Give the extent of all Plasmodium ovale-infected red blood cells.
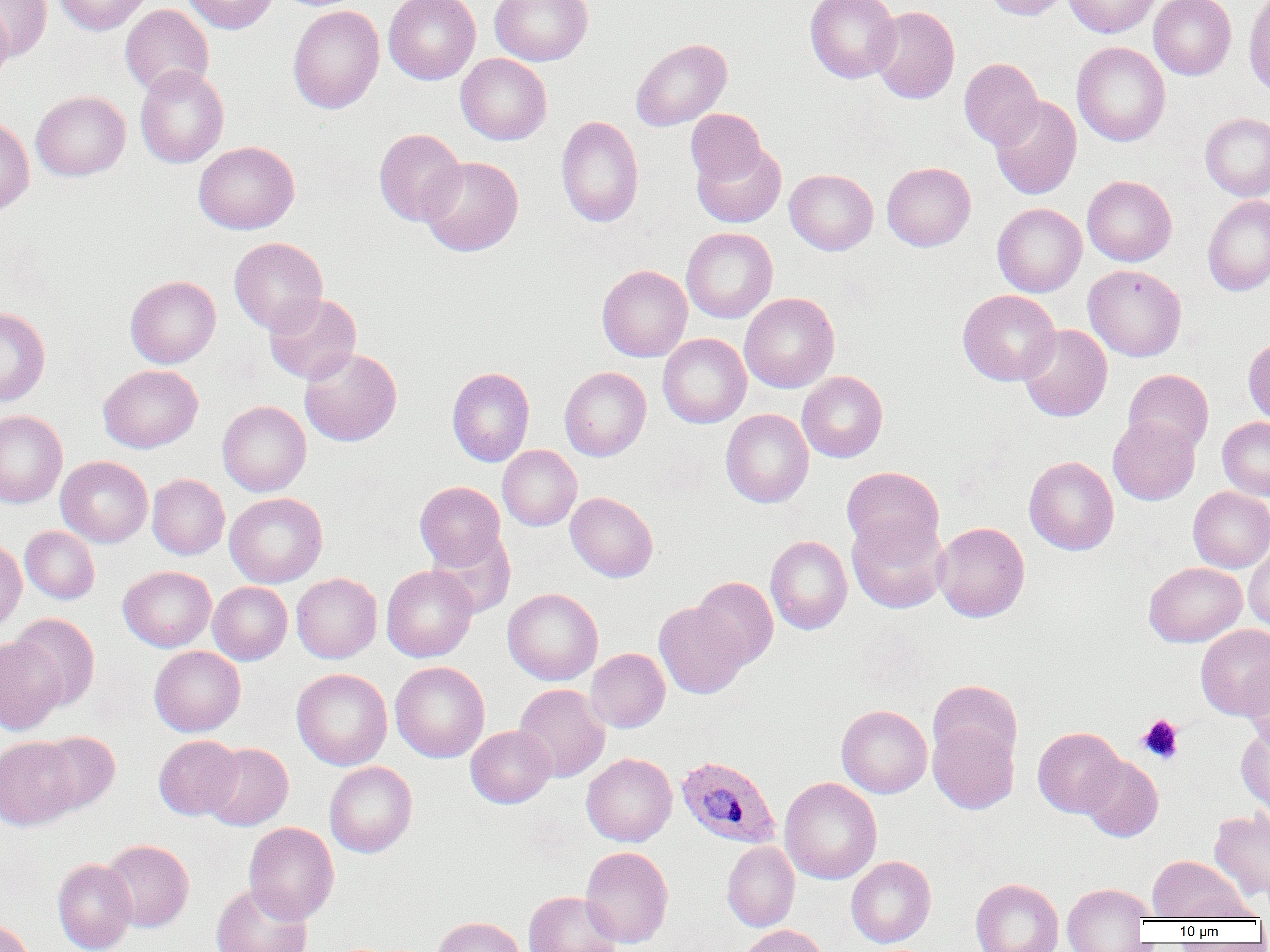
Approximate bounding boxes as (x1,y1)-(x2,y2) corner pairs in pixels.
Plasmodium ovale-infected red blood cells: (676,755)-(781,848).

slide-level diagnosis = Plasmodium ovale
magnification = 1000x
modality = optical microscopy
preparation = thin blood smear
platelet locations = approximate bounding boxes as (x1,y1)-(x2,y2) corner pairs in pixels: (1137,715)-(1184,764)
uninfected red blood cell locations = approximate bounding boxes as (x1,y1)-(x2,y2) corner pairs in pixels: (1,0)-(52,60), (53,0)-(151,35), (182,0)-(278,33), (384,0)-(480,84), (490,0)-(593,66), (805,0)-(901,83), (984,0)-(1070,20), (1062,0)-(1160,37), (1148,0)-(1236,80), (1243,0)-(1270,98), (120,4)-(214,97), (288,5)-(384,113), (868,6)-(959,103), (0,7)-(14,85), (630,38)-(731,131), (1071,42)-(1170,146), (456,53)-(551,145), (959,58)-(1043,149), (135,65)-(229,168), (31,90)-(130,181), (989,95)-(1081,200), (686,109)-(766,186), (1200,112)-(1270,201), (0,115)-(35,215), (556,116)-(644,227), (374,128)-(465,226), (194,141)-(300,234), (692,143)-(786,227), (419,156)-(523,256), (882,162)-(976,252), (785,169)-(878,255), (1082,176)-(1177,266), (1203,195)-(1270,296), (992,203)-(1087,296), (681,227)-(778,323), (229,237)-(328,334), (597,264)-(692,362), (1083,264)-(1186,362), (125,275)-(221,368), (957,289)-(1061,385), (263,292)-(361,384), (739,293)-(839,393), (0,307)-(50,406), (1018,324)-(1112,422), (658,334)-(751,428), (1243,336)-(1270,427), (299,347)-(402,446), (98,364)-(203,453), (447,367)-(535,467), (559,367)-(651,461), (1123,369)-(1213,455), (797,371)-(887,462), (217,400)-(311,496), (721,409)-(813,508), (0,410)-(67,507), (1108,417)-(1200,505), (1218,417)-(1270,500), (498,445)-(582,531), (56,456)-(153,548), (1024,456)-(1119,555), (842,466)-(945,559), (147,474)-(229,560), (415,481)-(505,570), (1188,487)-(1270,572), (224,492)-(328,587), (565,492)-(658,582), (847,516)-(948,614), (932,521)-(1030,622), (20,526)-(100,604), (428,530)-(516,618), (766,536)-(852,635), (0,539)-(26,634), (1244,541)-(1270,633), (1144,562)-(1247,646), (381,564)-(477,662), (118,565)-(216,651), (292,573)-(382,663), (691,576)-(778,670), (208,581)-(292,665), (503,588)-(603,685), (654,601)-(748,698), (10,614)-(100,710), (1195,624)-(1270,719), (0,637)-(66,735), (149,645)-(245,737), (586,648)-(670,733), (1240,659)-(1269,752), (390,661)-(490,762), (291,668)-(392,770), (928,680)-(1022,768), (513,684)-(610,782), (836,705)-(932,798), (928,720)-(1019,814), (1235,725)-(1270,817), (465,726)-(556,808), (1033,727)-(1125,817), (34,731)-(120,815), (154,735)-(243,819), (0,737)-(81,830), (202,743)-(293,830), (581,753)-(677,847), (1079,754)-(1163,842), (324,761)-(417,857), (780,777)-(882,885), (1209,807)-(1270,902), (243,822)-(339,924), (101,840)-(193,932), (722,841)-(799,931), (580,846)-(674,948), (846,856)-(936,947), (1148,856)-(1247,921), (52,858)-(137,952), (970,878)-(1063,952), (210,882)-(312,952), (1062,882)-(1153,951), (524,891)-(622,952), (1177,893)-(1266,923), (432,916)-(526,952), (0,919)-(34,952), (738,923)-(829,952)
image size = 1270×952 pixels
field of view = single